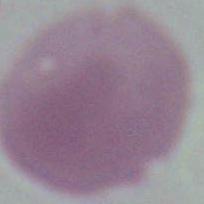
modality = photomicrograph
magnification = 1000x
identification = erythrocyte